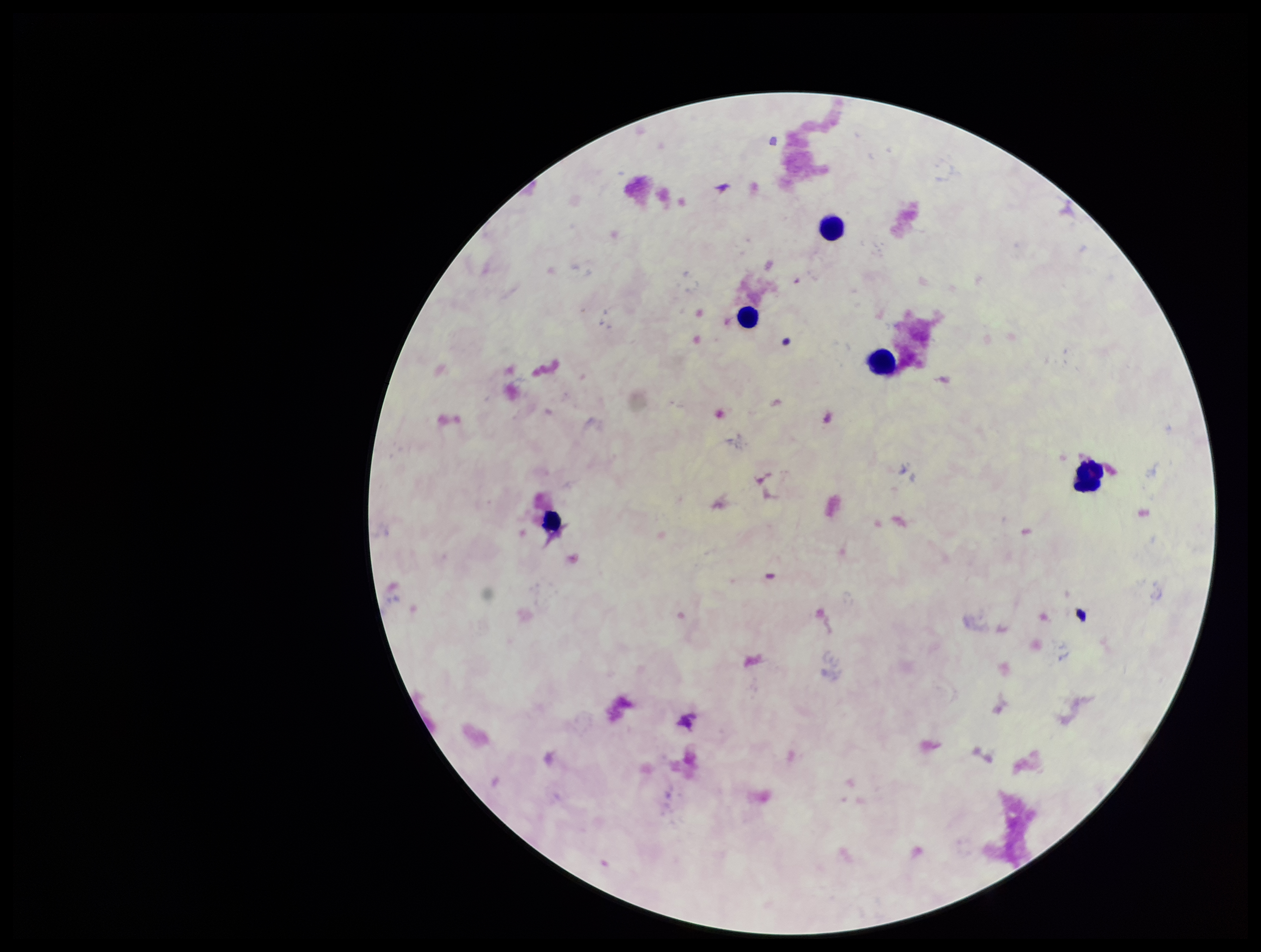
Parasite count: 0. Single field of view. Patient malaria status: negative. Giemsa stain. Smartphone photograph taken through the eyepiece of a microscope. Plasmodium parasites: none identified. Image is 1261×952 pixels. Leukocyte count: 5. Preparation: thick.